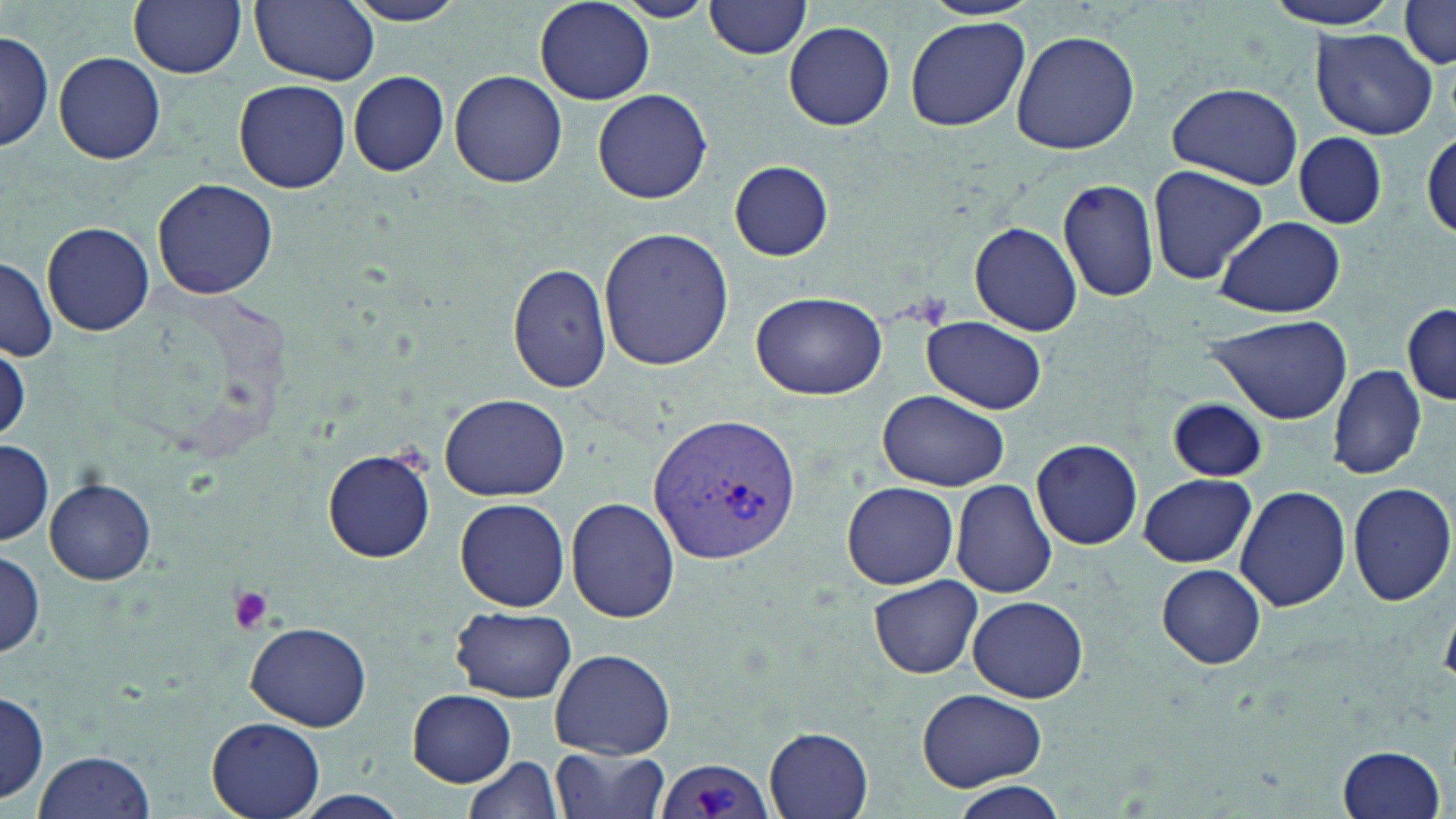

Approximate bounding boxes as (x1,y1)-(x2,y2) corner pairs in pixels. Uninfected red blood cell locations: (129,0)-(246,78), (250,0)-(379,84), (341,0)-(470,26), (615,0)-(715,23), (705,0)-(813,59), (1261,0)-(1408,30), (534,1)-(655,104), (1395,6)-(1456,71), (904,17)-(1029,131), (783,20)-(895,129), (1011,29)-(1141,156), (0,30)-(54,154), (1311,30)-(1436,139), (54,52)-(166,166), (449,70)-(567,188), (349,71)-(449,176), (234,80)-(351,194), (1166,80)-(1304,188), (592,88)-(712,204), (1291,130)-(1388,231), (1421,130)-(1455,245), (729,161)-(833,260), (1146,166)-(1268,285), (1057,175)-(1163,304), (152,177)-(277,299), (969,196)-(1158,313), (1212,216)-(1346,318), (43,221)-(153,336), (969,221)-(1082,336), (597,227)-(735,370), (1,257)-(56,362), (507,260)-(612,395), (750,290)-(888,400), (1401,300)-(1455,407), (1205,312)-(1353,424), (920,315)-(1047,415), (0,341)-(29,441), (1327,364)-(1427,481), (877,390)-(1010,492), (437,395)-(570,499), (1167,398)-(1267,482), (1031,437)-(1142,551), (0,440)-(52,545), (323,448)-(437,563), (1136,474)-(1258,568), (45,478)-(156,586), (951,479)-(1058,599), (843,482)-(959,588), (1347,482)-(1456,607), (1237,485)-(1353,614), (568,498)-(679,624), (454,499)-(570,611), (0,549)-(45,660), (1158,565)-(1266,669), (868,577)-(983,678), (967,596)-(1088,703), (451,606)-(576,703), (244,620)-(370,730), (549,648)-(675,758), (408,689)-(517,785), (916,689)-(1047,789), (0,692)-(48,805), (206,715)-(326,819), (764,727)-(875,817), (1335,743)-(1446,819), (551,745)-(670,819), (31,750)-(156,819), (462,755)-(565,819), (950,784)-(1068,818). Plasmodium vivax-infected red blood cell locations: (644,413)-(802,567), (654,758)-(775,819). Platelet locations: (224,584)-(276,636). Slide-level diagnosis: Plasmodium vivax. Light microscopy. Single field of view. 1000x magnification. Thin blood film. May-Grünwald-Giemsa-stained preparation. Image is 1456×819 pixels.